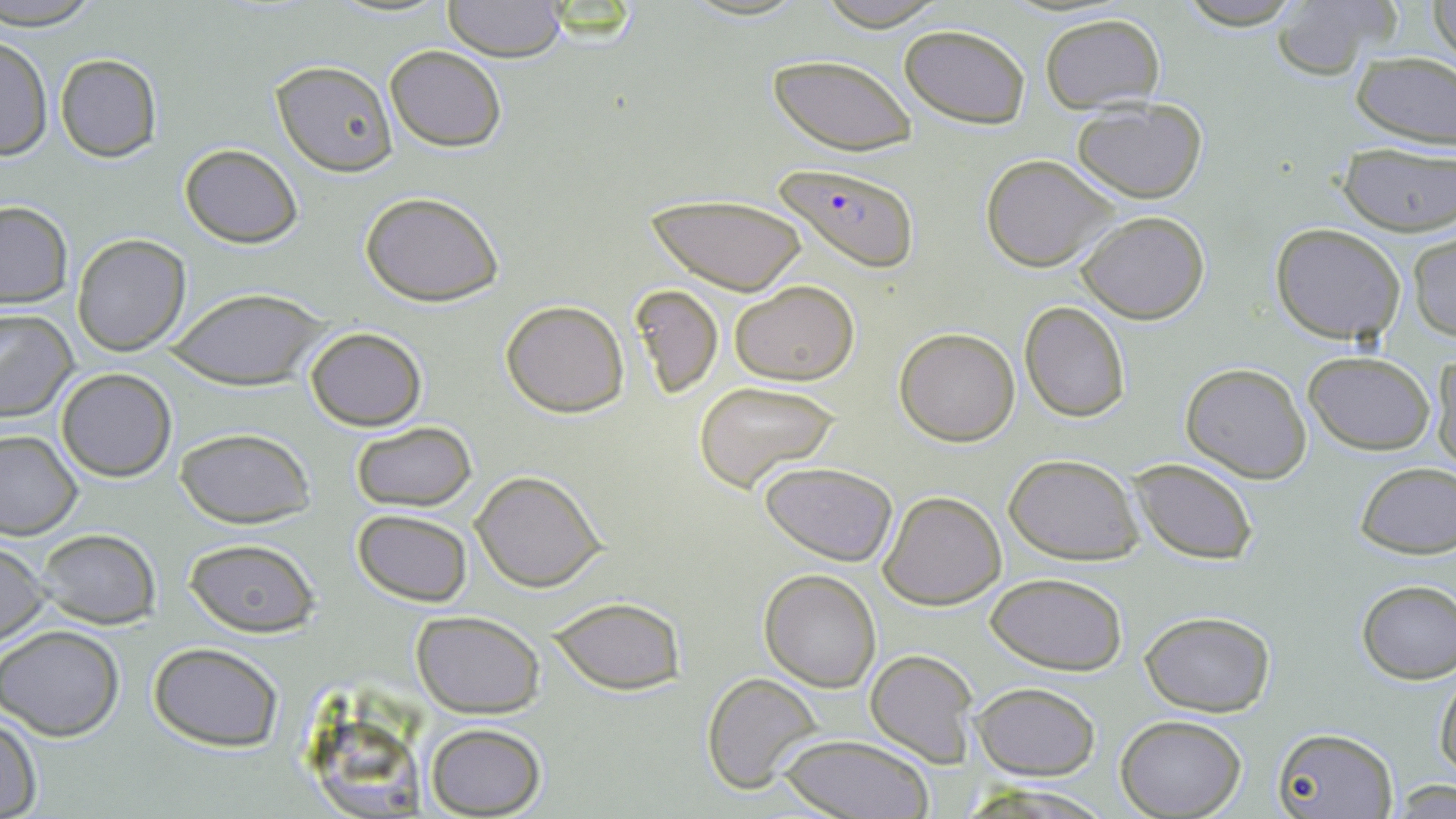

slide_level_diagnosis: Plasmodium falciparum
stain: May-Grünwald-Giemsa
uninfected_red_blood_cell_locations: 'approximate bounding boxes as [x1, y1, x2, y2] in pixels: [0, 0, 105, 30], [813, 0, 953, 30], [1173, 0, 1306, 29], [1430, 0, 1455, 67], [441, 1, 568, 61], [1267, 2, 1400, 81], [1039, 13, 1166, 111], [901, 23, 1030, 128], [1, 33, 51, 162], [384, 44, 506, 150], [1351, 51, 1456, 149], [55, 54, 162, 163], [768, 54, 918, 156], [270, 59, 397, 175], [1071, 99, 1210, 201], [180, 144, 302, 247], [1338, 145, 1456, 234], [980, 155, 1118, 273], [361, 191, 504, 307], [646, 192, 809, 295], [0, 201, 73, 308], [1078, 210, 1210, 324], [1271, 223, 1407, 346], [1408, 231, 1456, 342], [72, 233, 192, 355], [730, 282, 858, 383], [629, 283, 723, 398], [166, 291, 327, 388], [501, 299, 629, 418], [1019, 300, 1131, 422], [0, 308, 76, 423], [305, 326, 427, 431], [894, 327, 1020, 445], [1430, 350, 1456, 471], [1302, 352, 1435, 455], [1180, 362, 1313, 482], [56, 367, 176, 480], [693, 380, 843, 493], [350, 421, 477, 511], [174, 428, 316, 527], [0, 429, 82, 539], [1006, 456, 1144, 565], [1128, 457, 1258, 565], [1354, 461, 1456, 558], [758, 462, 898, 566], [471, 470, 604, 591], [877, 491, 1005, 610], [352, 509, 473, 605], [34, 528, 160, 629], [183, 538, 320, 638], [0, 541, 52, 646], [759, 569, 881, 691], [986, 573, 1127, 674], [1355, 580, 1456, 683], [551, 599, 683, 693], [412, 610, 544, 715], [1140, 610, 1276, 716], [0, 624, 126, 742], [149, 642, 284, 751], [864, 649, 978, 765], [1435, 663, 1456, 782], [701, 672, 824, 793], [973, 682, 1101, 780], [0, 712, 42, 819], [314, 714, 422, 819], [1117, 715, 1246, 818], [423, 722, 547, 817], [1273, 726, 1395, 817], [778, 734, 936, 818], [1389, 780, 1454, 818], [963, 784, 1115, 817]'
plasmodium_falciparum_infected_red_blood_cell_locations: 'approximate bounding boxes as [x1, y1, x2, y2] in pixels: [777, 163, 920, 271]'
magnification: 1000x
field_of_view: single
preparation: thin blood film
modality: light microscopy
image_size: 1456×819 pixels